Identify the parasite.
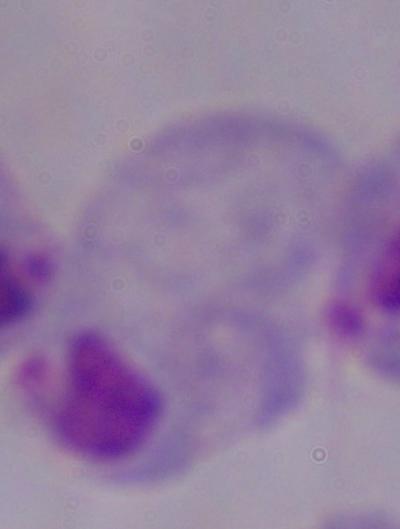
A trichomonad.

Summary:
  - Magnification: 1000x
  - Modality: micrograph